Classify this cell by malaria status.
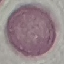
Uninfected.

capture: smartphone camera at the microscope eyepiece
stain: Giemsa
image_type: cell patch, automatically extracted from a larger field of view and resized to 64 × 64 pixels
preparation: thin smear